Report the malaria status of this cell.
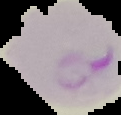
It is parasitized.

Summary:
  - Image size: 121×115 pixels
  - Image type: cell region segmented out of the field of view; surrounding area masked to black
  - Preparation: thin blood film